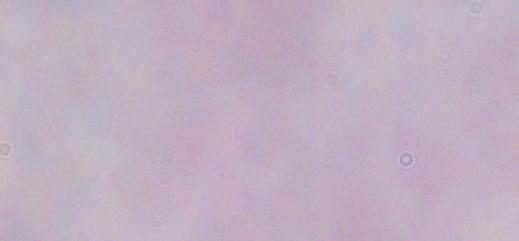

magnification: 1000x
modality: micrograph
identification: trypanosome